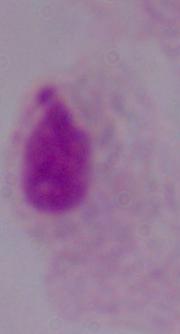
Summary:
  - Magnification: 1000x
  - Modality: micrograph
  - Identification: trichomonad